Comment on the morphology of the erythrocytes.
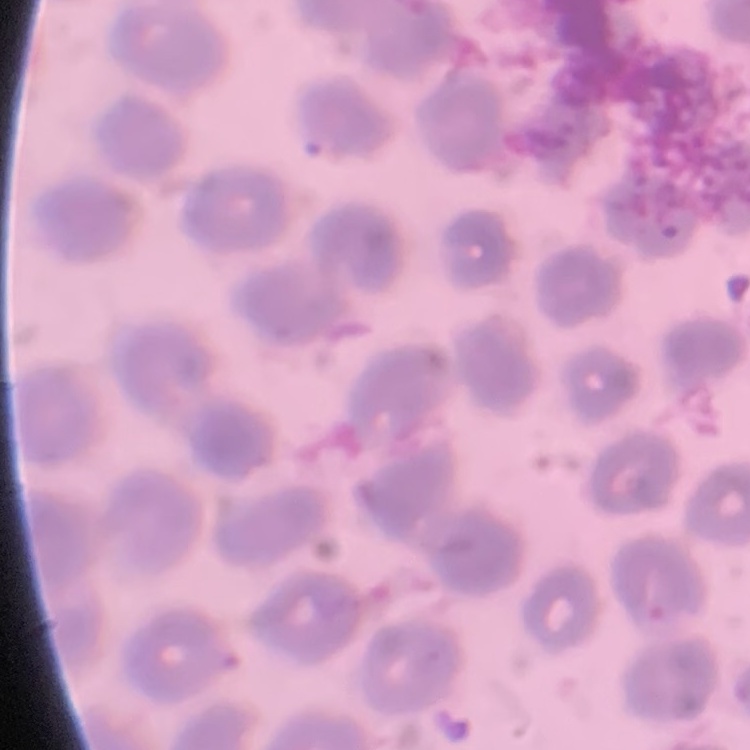

They show no rouleaux formation.

One tile cut from a larger photomicrograph. Field's or Giemsa stain. Thin blood film.